Give a bounding box for every Plasmodium parasite.
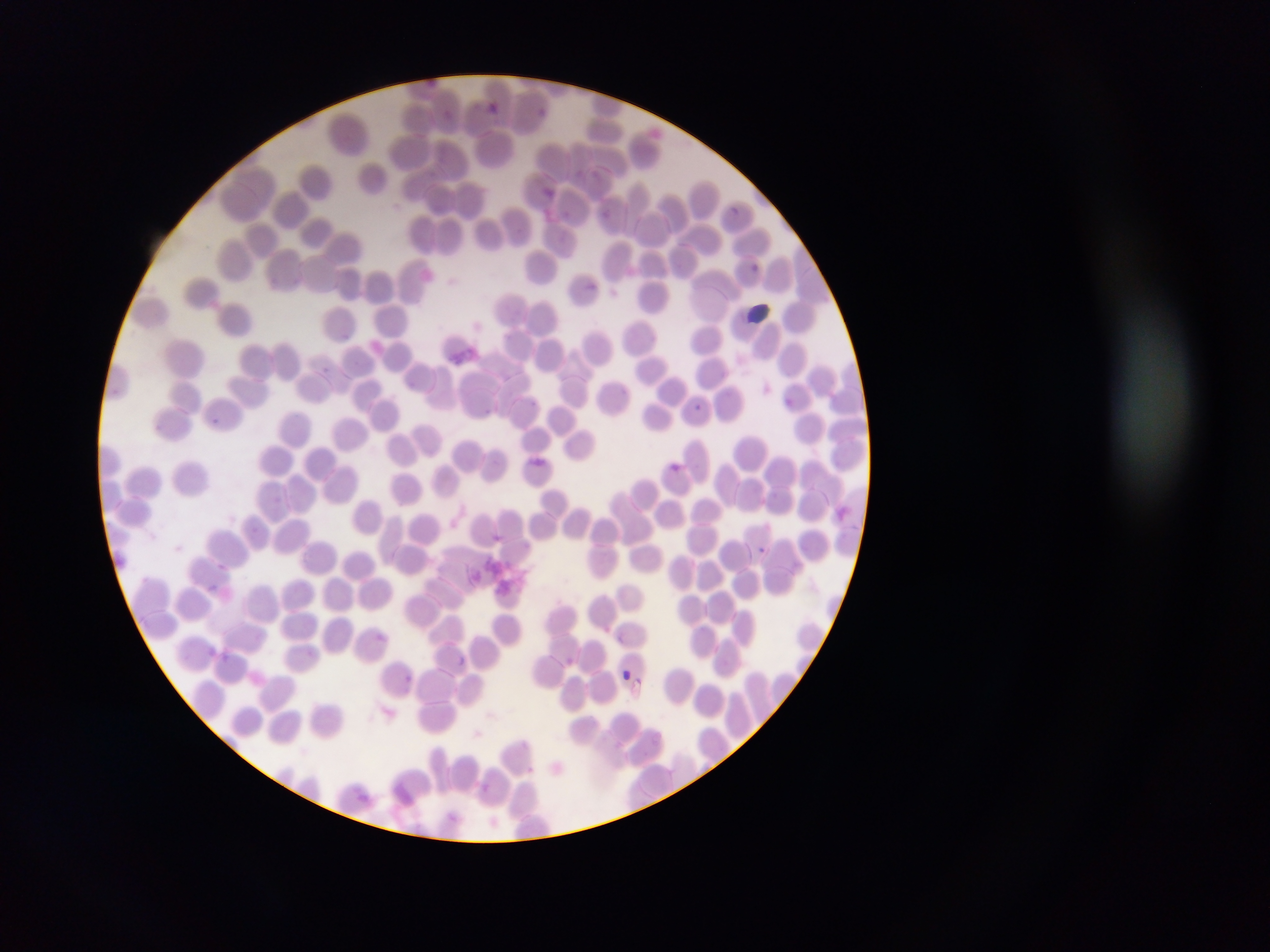
Approximate bounding boxes as [left, top, right, bottom] in pixels.
Plasmodium parasites: [479, 99, 507, 123], [727, 205, 743, 219], [750, 262, 768, 277], [778, 396, 799, 414], [688, 401, 707, 417], [211, 412, 219, 425], [666, 460, 700, 478], [754, 545, 769, 559], [207, 582, 227, 597], [369, 630, 387, 647], [612, 631, 629, 649], [206, 635, 221, 654], [442, 636, 456, 650], [563, 655, 581, 668], [458, 658, 473, 668], [617, 666, 637, 685], [405, 674, 415, 683].

Summary:
  - Leukocyte locations: [741, 302, 779, 326]
  - Artifact (stain precipitate or debris) locations: [474, 548, 529, 597]
  - Field of view: single
  - Preparation: thin blood film
  - Country: Ghana
  - Capture: mobile-phone photograph through a microscope
  - Image size: 1270×952 pixels